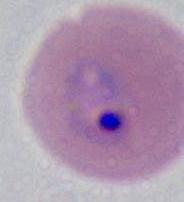

Summary:
  - Identification: Plasmodium
  - Magnification: 400x or 1000x
  - Modality: photomicrograph